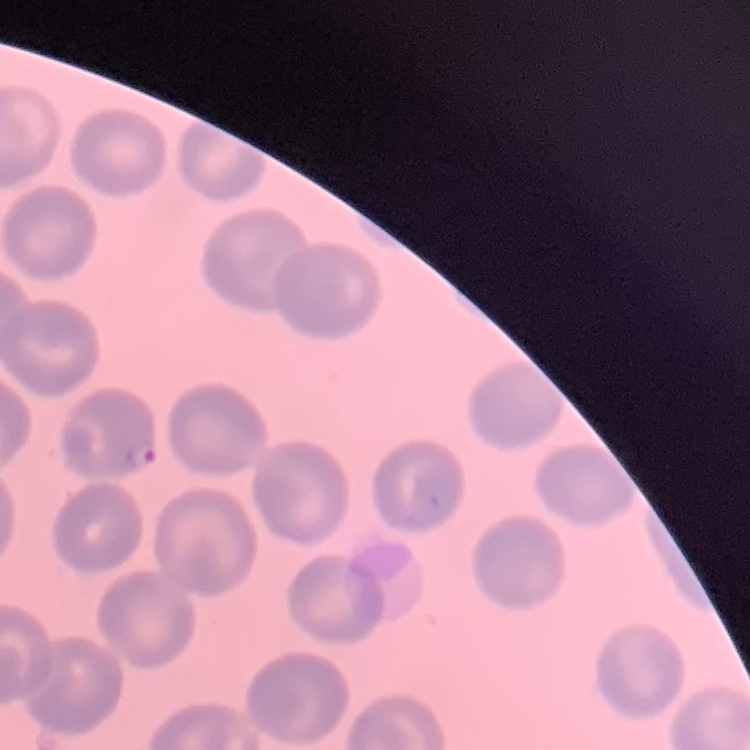

erythrocyte_morphology: no rouleaux formation
stain: Field's or Giemsa
preparation: thin blood smear
image_type: square crop of a larger photomicrograph